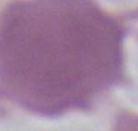
Summary:
  - Modality: photomicrograph
  - Magnification: 1000x
  - Identification: erythrocyte